Name the cell type shown.
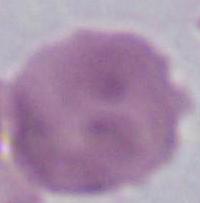

An erythrocyte.

Photomicrograph. 1000x magnification.